Assess the morphology of the erythrocytes.
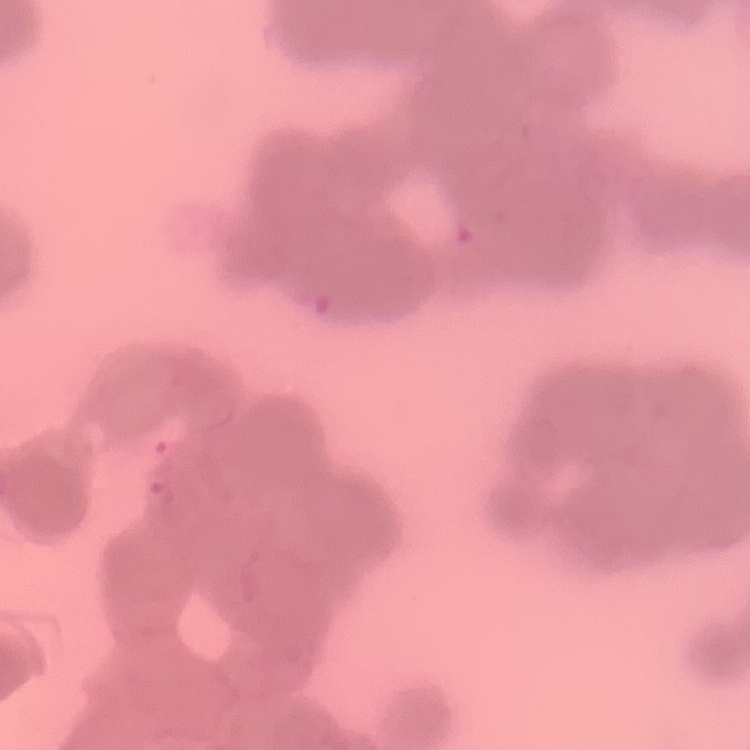

They show rouleaux formation.

image_type: one tile cut from a larger photomicrograph
preparation: thin blood film
stain: Field's or Giemsa